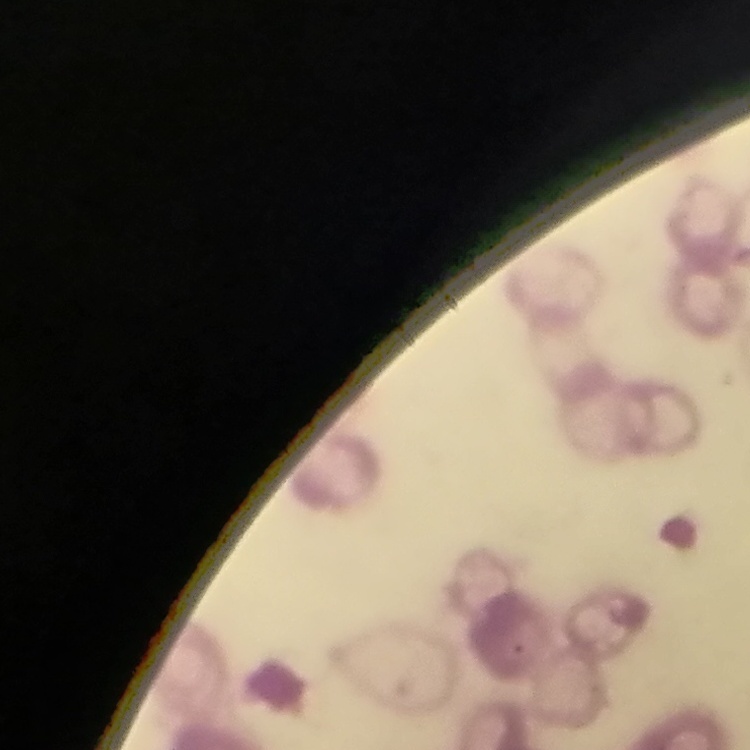
The red blood cells show rouleaux formation. Thin peripheral smear. Field's or Giemsa stain. Square crop of a larger photomicrograph.